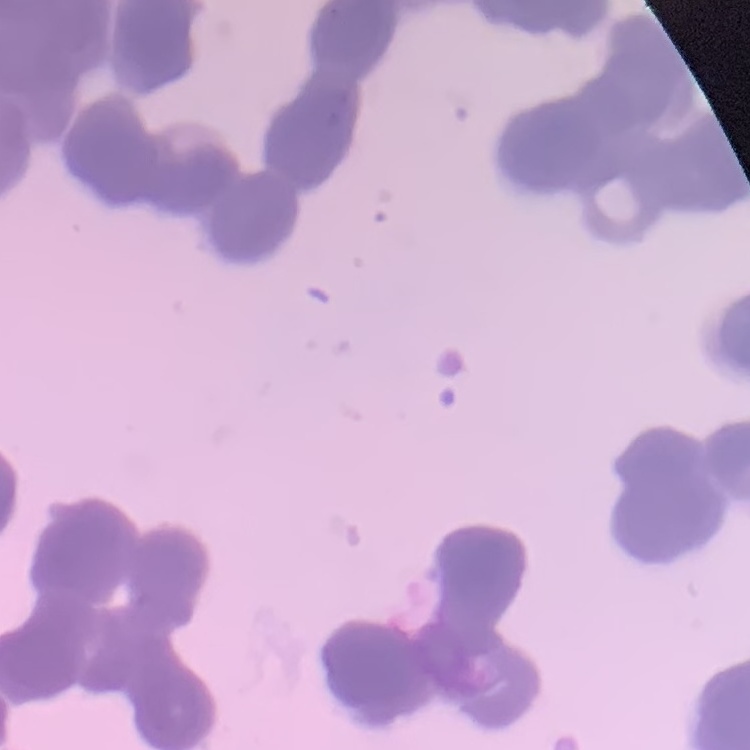

The erythrocytes exhibit rouleaux formation. Stained with either Field's or Giemsa. Thin peripheral smear. Square crop of a larger photomicrograph.